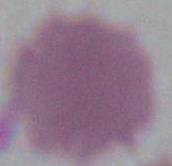
Summary:
  - Modality: micrograph
  - Identification: erythrocyte
  - Magnification: 1000x